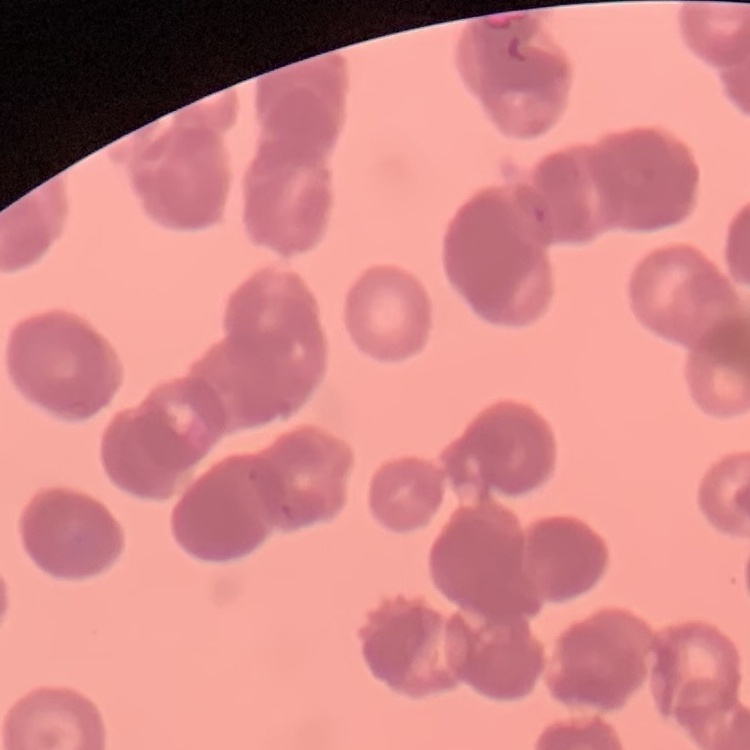

Summary:
  - Erythrocyte morphology: rouleaux formation
  - Stain: Field's or Giemsa
  - Image type: square crop of a larger photomicrograph
  - Preparation: thin peripheral smear